Locate every Plasmodium parasite and every leukocyte.
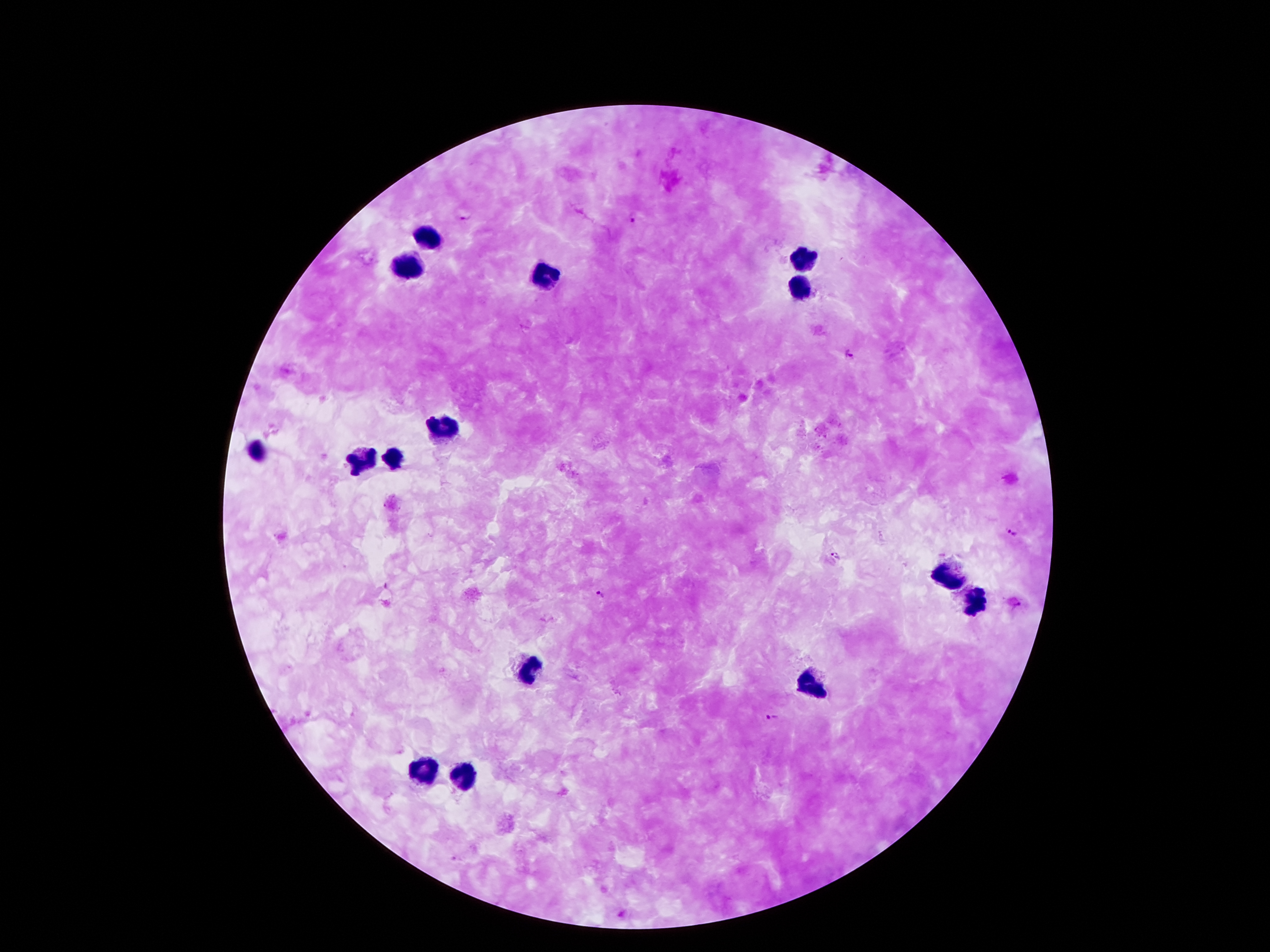

Approximate object centers, in pixels from the top-left corner.
Plasmodium parasites: (x=633, y=217), (x=467, y=219), (x=849, y=355), (x=1011, y=532), (x=835, y=555), (x=602, y=594), (x=770, y=718).
Leukocytes: (x=423, y=237), (x=804, y=259), (x=410, y=270), (x=543, y=274), (x=798, y=283), (x=444, y=429), (x=261, y=451), (x=397, y=457), (x=362, y=463), (x=944, y=573), (x=977, y=602), (x=527, y=670), (x=811, y=680), (x=426, y=772), (x=467, y=774).

Summary:
  - Image size: 1270×952 pixels
  - Capture: smartphone camera through the microscope eyepiece
  - Patient malaria status: positive for Plasmodium falciparum
  - Field of view: single
  - Stain: Giemsa
  - Preparation: thick blood smear
  - Magnification: 100x